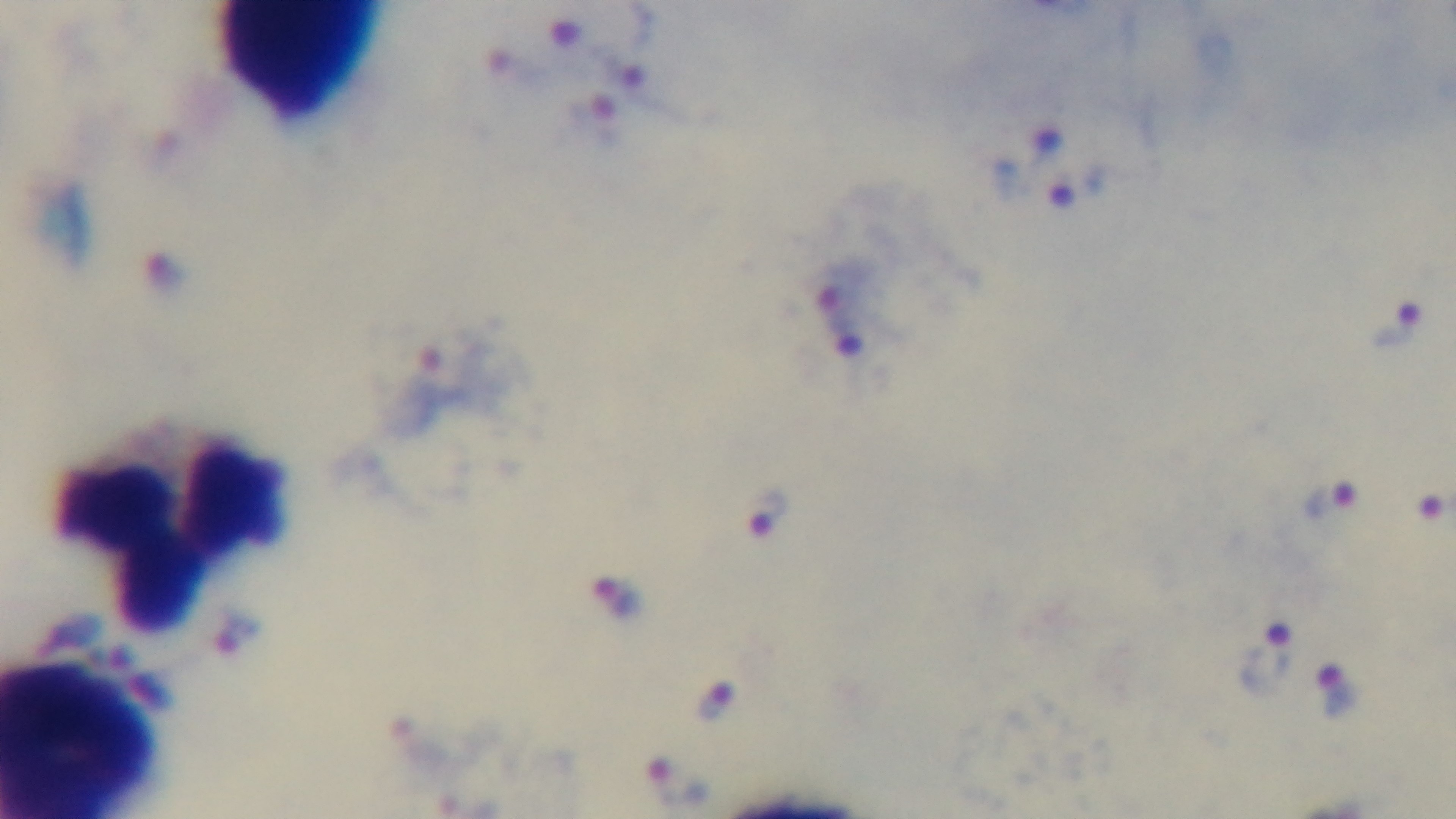

Summary:
  - Field of view: single
  - Capture: mounted 4K digital camera
  - Preparation: thick blood film
  - Malaria status: infected
  - Modality: light microscopy
  - Objective: 100x oil immersion
  - Stain: Giemsa